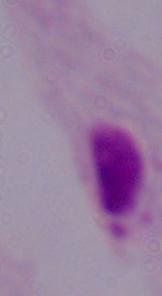

{
  "magnification": "1000x",
  "identification": "trichomonad",
  "modality": "photomicrograph"
}